Identify the cell.
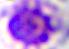

This is a leukocyte.

Summary:
  - Magnification: 400x
  - Modality: micrograph